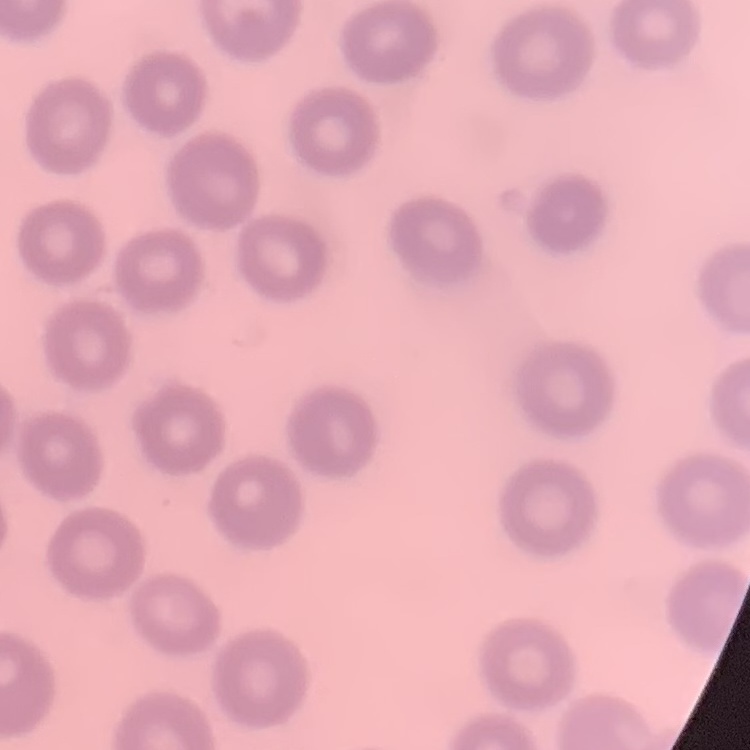
{
  "erythrocyte_morphology": "no rouleaux formation",
  "preparation": "thin blood film",
  "stain": "Field's or Giemsa",
  "image_type": "one tile cut from a larger photomicrograph"
}